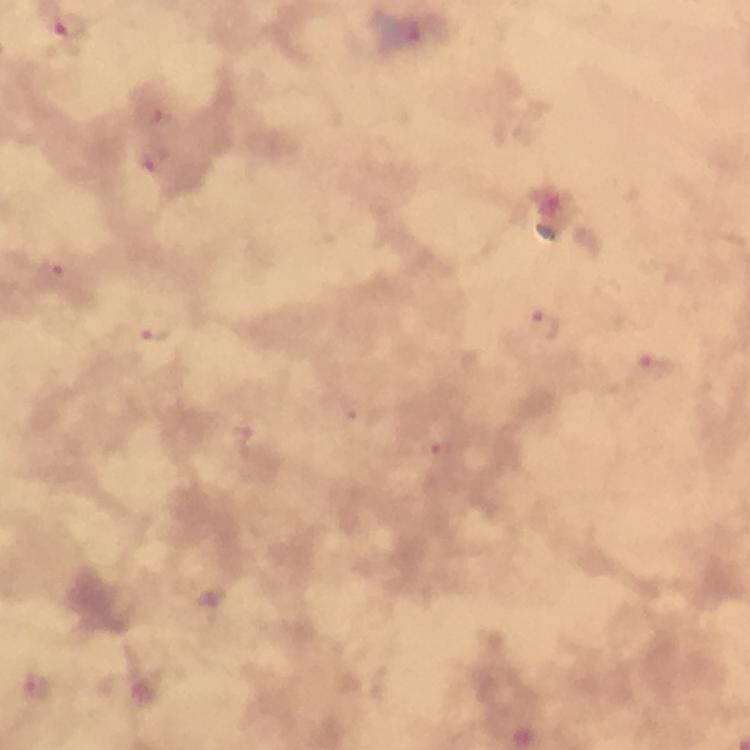

Plasmodium parasite locations = approximate centers as [x, y] in pixels: [69, 24], [156, 119], [152, 159], [57, 264], [544, 324], [150, 327], [652, 367], [242, 440], [435, 453], [37, 687]
magnification = 100x
image size = 750×750 pixels
stain = Giemsa
immersion oil = used
context = from a malaria diagnostic workup
cropped from = one field of view
capture = smartphone photograph through a microscope
preparation = thick blood smear